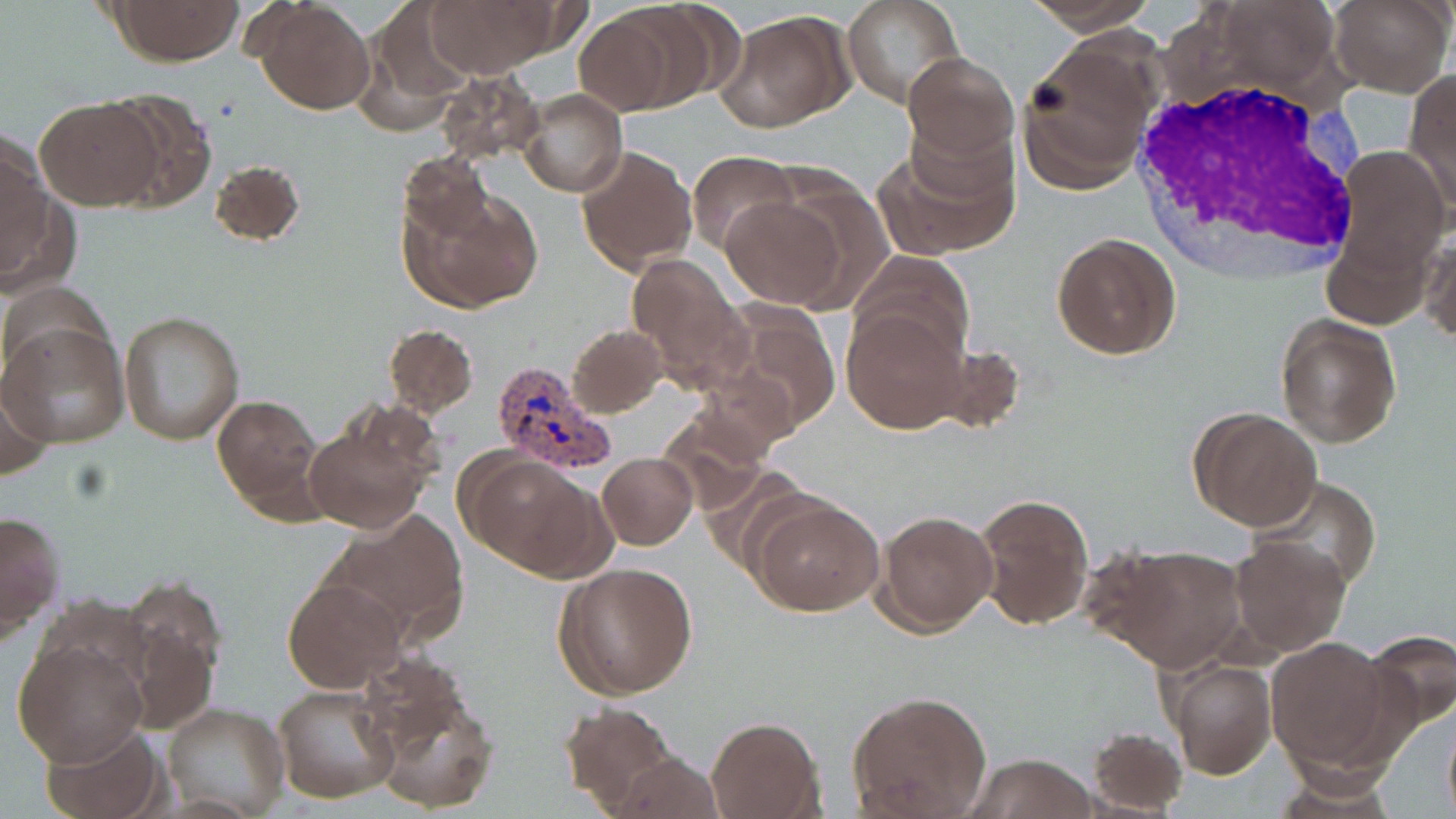

Approximate bounding boxes as (x1,y1)-(x2,y2) corner pairs in pixels. Uninfected red blood cell locations: (109,0)-(243,66), (257,0)-(374,116), (420,0)-(564,77), (842,0)-(964,109), (1021,0)-(1162,36), (1330,0)-(1454,97), (614,2)-(736,111), (358,8)-(473,131), (572,9)-(685,113), (718,11)-(852,131), (1020,45)-(1153,192), (901,51)-(1017,165), (437,70)-(545,165), (1404,71)-(1456,208), (517,87)-(628,197), (100,90)-(216,212), (35,97)-(162,211), (877,133)-(1018,260), (1,137)-(56,274), (1334,144)-(1449,277), (576,145)-(697,276), (687,150)-(800,257), (397,153)-(493,242), (210,159)-(305,248), (767,173)-(896,311), (398,187)-(544,312), (718,197)-(845,308), (1323,230)-(1432,330), (1051,232)-(1181,359), (1420,232)-(1455,346), (851,252)-(976,361), (626,254)-(752,390), (709,301)-(842,439), (842,305)-(967,434), (117,310)-(245,446), (1274,313)-(1403,450), (1,322)-(129,449), (382,324)-(479,417), (567,324)-(667,419), (0,371)-(57,483), (212,396)-(320,509), (1189,407)-(1322,531), (656,409)-(770,514), (300,415)-(439,537), (461,452)-(598,575), (597,453)-(697,549), (1251,476)-(1384,595), (970,491)-(1093,632), (748,493)-(883,616), (0,509)-(66,640), (874,509)-(997,636), (324,512)-(469,641), (1227,535)-(1353,657), (1097,542)-(1248,673), (553,561)-(700,700), (282,576)-(406,694), (120,585)-(222,728), (1355,629)-(1456,735), (1265,636)-(1394,769), (12,640)-(148,767), (1161,655)-(1277,780), (361,664)-(499,812), (273,685)-(398,804), (847,689)-(993,817), (557,701)-(681,815), (161,703)-(290,819), (1442,712)-(1455,819), (706,717)-(822,819), (41,723)-(165,818), (1087,726)-(1188,815), (610,752)-(726,818), (967,752)-(1099,819), (1268,760)-(1398,815). White blood cell locations: (1128,72)-(1371,277). Plasmodium vivax-infected red blood cell locations: (490,358)-(617,476). Slide-level diagnosis: Plasmodium vivax. May-Grünwald-Giemsa stain. Captured at 1000x magnification. Thin blood smear. Image is 1456×819 pixels. Light microscopy. Single field of view.